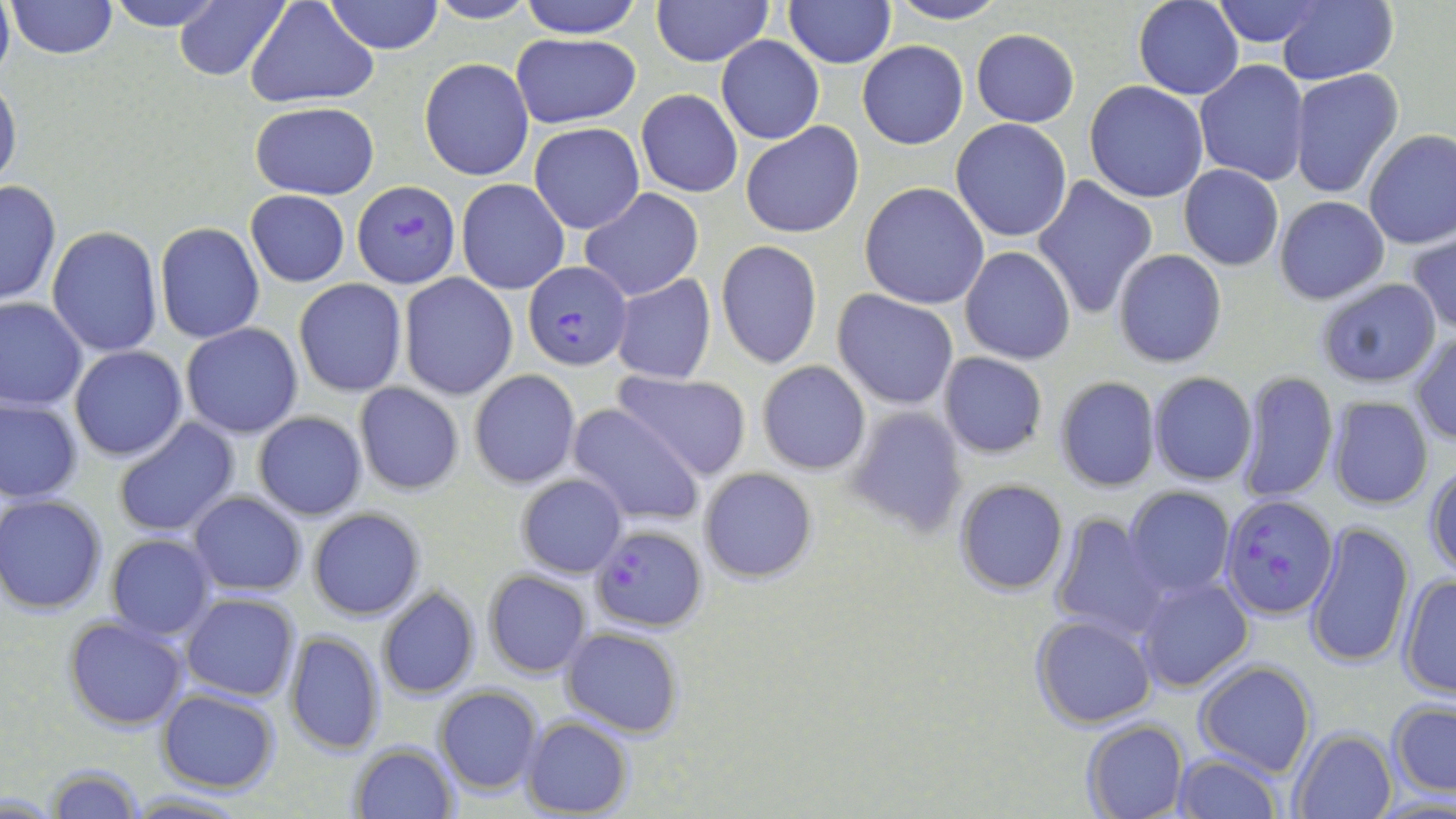

Summary:
  - Coordinate format: approximate bounding boxes as named x1/y1/x2/y2 corners in pixels
  - Uninfected red blood cell locations: (x1=102, y1=0, x2=225, y2=31), (x1=323, y1=0, x2=444, y2=54), (x1=423, y1=0, x2=539, y2=25), (x1=518, y1=0, x2=645, y2=38), (x1=651, y1=0, x2=773, y2=66), (x1=886, y1=0, x2=1009, y2=25), (x1=1213, y1=0, x2=1327, y2=47), (x1=1276, y1=0, x2=1398, y2=84), (x1=4, y1=1, x2=120, y2=59), (x1=246, y1=1, x2=379, y2=107), (x1=785, y1=1, x2=895, y2=67), (x1=1132, y1=1, x2=1243, y2=100), (x1=174, y1=2, x2=287, y2=81), (x1=971, y1=29, x2=1080, y2=127), (x1=510, y1=33, x2=642, y2=128), (x1=716, y1=35, x2=823, y2=144), (x1=857, y1=41, x2=968, y2=149), (x1=420, y1=57, x2=534, y2=180), (x1=1194, y1=59, x2=1309, y2=186), (x1=1288, y1=69, x2=1403, y2=198), (x1=0, y1=76, x2=21, y2=194), (x1=1084, y1=81, x2=1209, y2=203), (x1=636, y1=89, x2=743, y2=198), (x1=249, y1=101, x2=380, y2=200), (x1=951, y1=118, x2=1073, y2=243), (x1=740, y1=122, x2=864, y2=239), (x1=530, y1=123, x2=644, y2=233), (x1=1363, y1=129, x2=1456, y2=248), (x1=1178, y1=165, x2=1284, y2=270), (x1=1032, y1=175, x2=1159, y2=321), (x1=456, y1=178, x2=569, y2=295), (x1=1, y1=180, x2=61, y2=306), (x1=859, y1=182, x2=989, y2=310), (x1=579, y1=188, x2=704, y2=301), (x1=246, y1=189, x2=349, y2=287), (x1=1274, y1=196, x2=1390, y2=305), (x1=154, y1=221, x2=265, y2=344), (x1=46, y1=225, x2=163, y2=358), (x1=1406, y1=232, x2=1456, y2=336), (x1=716, y1=241, x2=823, y2=368), (x1=959, y1=246, x2=1076, y2=364), (x1=1111, y1=248, x2=1227, y2=369), (x1=399, y1=274, x2=518, y2=400), (x1=609, y1=274, x2=717, y2=385), (x1=1315, y1=277, x2=1440, y2=389), (x1=294, y1=278, x2=407, y2=396), (x1=832, y1=290, x2=960, y2=410), (x1=0, y1=297, x2=87, y2=409), (x1=181, y1=324, x2=303, y2=438), (x1=1409, y1=331, x2=1456, y2=445), (x1=69, y1=347, x2=189, y2=462), (x1=937, y1=352, x2=1048, y2=458), (x1=756, y1=359, x2=871, y2=475), (x1=469, y1=369, x2=581, y2=489), (x1=610, y1=369, x2=752, y2=480), (x1=1147, y1=371, x2=1257, y2=486), (x1=1234, y1=371, x2=1337, y2=503), (x1=1053, y1=377, x2=1161, y2=492), (x1=353, y1=382, x2=464, y2=496), (x1=0, y1=396, x2=84, y2=504), (x1=1326, y1=397, x2=1434, y2=510), (x1=568, y1=404, x2=705, y2=527), (x1=844, y1=406, x2=969, y2=538), (x1=253, y1=411, x2=367, y2=521), (x1=112, y1=416, x2=240, y2=538), (x1=1424, y1=463, x2=1456, y2=579), (x1=698, y1=467, x2=819, y2=584), (x1=515, y1=473, x2=629, y2=578), (x1=954, y1=479, x2=1070, y2=595), (x1=1123, y1=486, x2=1235, y2=598), (x1=188, y1=491, x2=307, y2=596), (x1=1, y1=495, x2=107, y2=614), (x1=309, y1=508, x2=425, y2=622), (x1=1048, y1=512, x2=1169, y2=643), (x1=1306, y1=520, x2=1415, y2=668), (x1=105, y1=534, x2=216, y2=639), (x1=482, y1=569, x2=592, y2=678), (x1=1133, y1=575, x2=1253, y2=693), (x1=1397, y1=575, x2=1456, y2=699), (x1=376, y1=588, x2=482, y2=699), (x1=181, y1=593, x2=300, y2=702), (x1=1029, y1=614, x2=1157, y2=731), (x1=64, y1=616, x2=190, y2=731), (x1=560, y1=626, x2=683, y2=737), (x1=286, y1=631, x2=385, y2=755), (x1=1194, y1=660, x2=1317, y2=777), (x1=434, y1=685, x2=544, y2=795), (x1=156, y1=688, x2=281, y2=794), (x1=1386, y1=698, x2=1455, y2=798), (x1=520, y1=717, x2=632, y2=818), (x1=1081, y1=719, x2=1189, y2=819), (x1=1288, y1=726, x2=1399, y2=819), (x1=351, y1=743, x2=457, y2=818), (x1=1168, y1=752, x2=1282, y2=819), (x1=45, y1=764, x2=144, y2=819), (x1=124, y1=791, x2=251, y2=819)
  - Plasmodium falciparum-infected red blood cell locations: (x1=352, y1=181, x2=461, y2=289), (x1=521, y1=261, x2=631, y2=370), (x1=1221, y1=494, x2=1338, y2=618), (x1=590, y1=525, x2=706, y2=633)
  - Slide-level diagnosis: Plasmodium falciparum
  - Modality: optical microscopy
  - Magnification: 1000x
  - Field of view: one of a larger specimen
  - Image size: 1456×819 pixels
  - Preparation: thin blood film
  - Stain: May-Grünwald-Giemsa